Locate every Plasmodium parasite and every leukocyte.
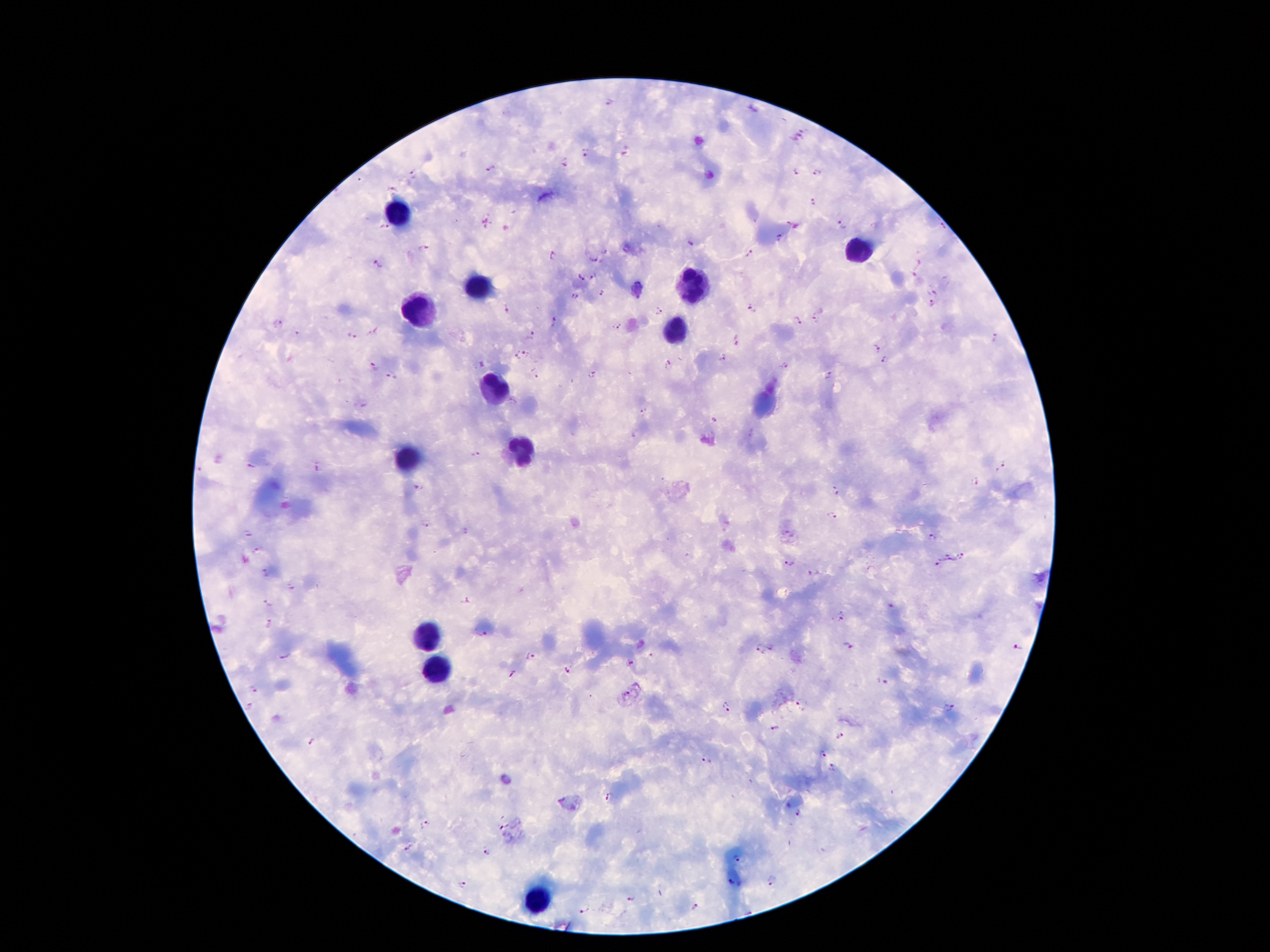
Approximate object centers, in pixels from the top-left corner.
Plasmodium parasites: (x=610, y=102), (x=798, y=138), (x=584, y=153), (x=565, y=163), (x=490, y=169), (x=413, y=171), (x=796, y=171), (x=817, y=173), (x=392, y=191), (x=813, y=200), (x=790, y=220), (x=841, y=225), (x=382, y=226), (x=780, y=238), (x=688, y=245), (x=424, y=249), (x=749, y=253), (x=552, y=255), (x=593, y=258), (x=919, y=262), (x=378, y=264), (x=593, y=274), (x=912, y=275), (x=580, y=277), (x=638, y=288), (x=936, y=291), (x=602, y=294), (x=574, y=296), (x=933, y=303), (x=752, y=308), (x=506, y=309), (x=659, y=312), (x=816, y=319), (x=552, y=321), (x=797, y=321), (x=278, y=323), (x=617, y=326), (x=375, y=332), (x=531, y=334), (x=353, y=338), (x=995, y=339), (x=736, y=342), (x=875, y=348), (x=528, y=352), (x=518, y=357), (x=722, y=357), (x=885, y=362), (x=480, y=364), (x=668, y=365), (x=784, y=365), (x=371, y=367), (x=535, y=372), (x=593, y=374), (x=827, y=376), (x=390, y=377), (x=644, y=410), (x=715, y=419), (x=477, y=454), (x=251, y=465), (x=1000, y=465), (x=317, y=468), (x=976, y=481), (x=418, y=489), (x=835, y=490), (x=833, y=516), (x=426, y=525), (x=464, y=531), (x=247, y=534), (x=931, y=537), (x=257, y=551), (x=960, y=556), (x=949, y=558), (x=940, y=564), (x=789, y=565), (x=266, y=573), (x=814, y=573), (x=290, y=588), (x=465, y=600), (x=268, y=603), (x=891, y=604), (x=840, y=619), (x=269, y=624), (x=483, y=635), (x=771, y=646), (x=848, y=646), (x=1016, y=648), (x=759, y=649), (x=650, y=656), (x=284, y=657), (x=531, y=657), (x=631, y=663), (x=567, y=670), (x=513, y=675), (x=881, y=681), (x=253, y=689), (x=623, y=695), (x=801, y=703), (x=247, y=707), (x=949, y=707), (x=727, y=708), (x=775, y=729), (x=840, y=736), (x=312, y=741), (x=821, y=755), (x=705, y=760), (x=833, y=767), (x=609, y=797), (x=798, y=816), (x=425, y=824), (x=498, y=825), (x=408, y=847), (x=487, y=850), (x=735, y=858), (x=730, y=881), (x=771, y=881), (x=462, y=883), (x=631, y=899), (x=696, y=906), (x=586, y=909).
Leukocytes: (x=396, y=215), (x=858, y=250), (x=690, y=286), (x=476, y=290), (x=419, y=307), (x=676, y=330), (x=495, y=387), (x=520, y=448), (x=407, y=458), (x=423, y=637), (x=440, y=672), (x=537, y=899).

Image is 1270×952 pixels. Patient malaria status: infected with Plasmodium falciparum. Giemsa stain. Single field of view. Smartphone photograph taken through the microscope eyepiece. Thick blood film. 100x magnification.